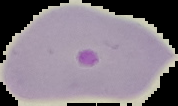 From a thin blood film. Malaria status: parasitized. Image is 178×106 pixels. Cell region segmented out of the field of view; the surrounding area is masked to black.